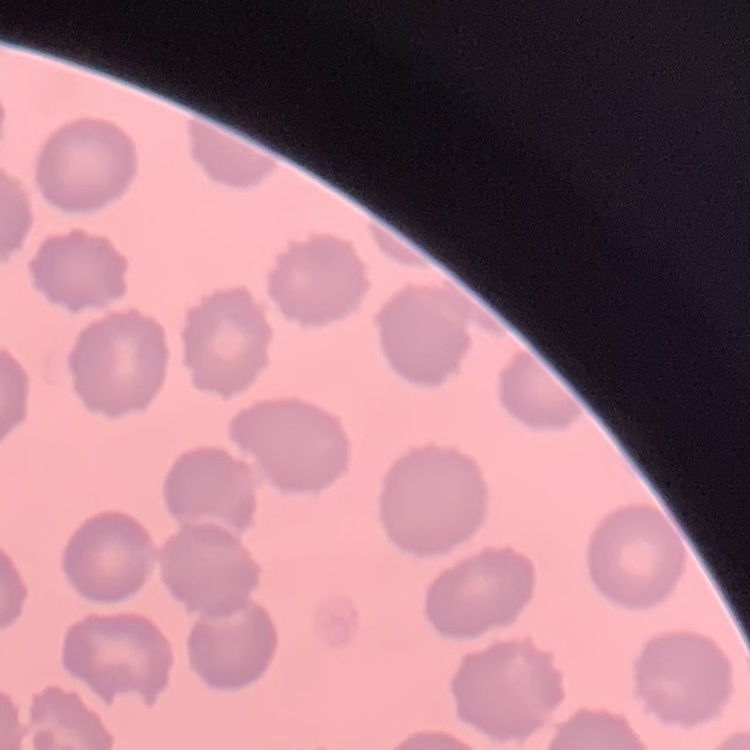

red_blood_cell_morphology: no rouleaux formation
image_type: square crop of a larger photomicrograph
stain: Field's or Giemsa
preparation: thin blood smear